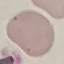

Summary:
  - Result: no malaria parasites seen
  - Preparation: thin blood smear
  - Capture: smartphone camera at the microscope eyepiece
  - Image type: automatically extracted cell patch, resized to 64 × 64 pixels
  - Stain: Giemsa